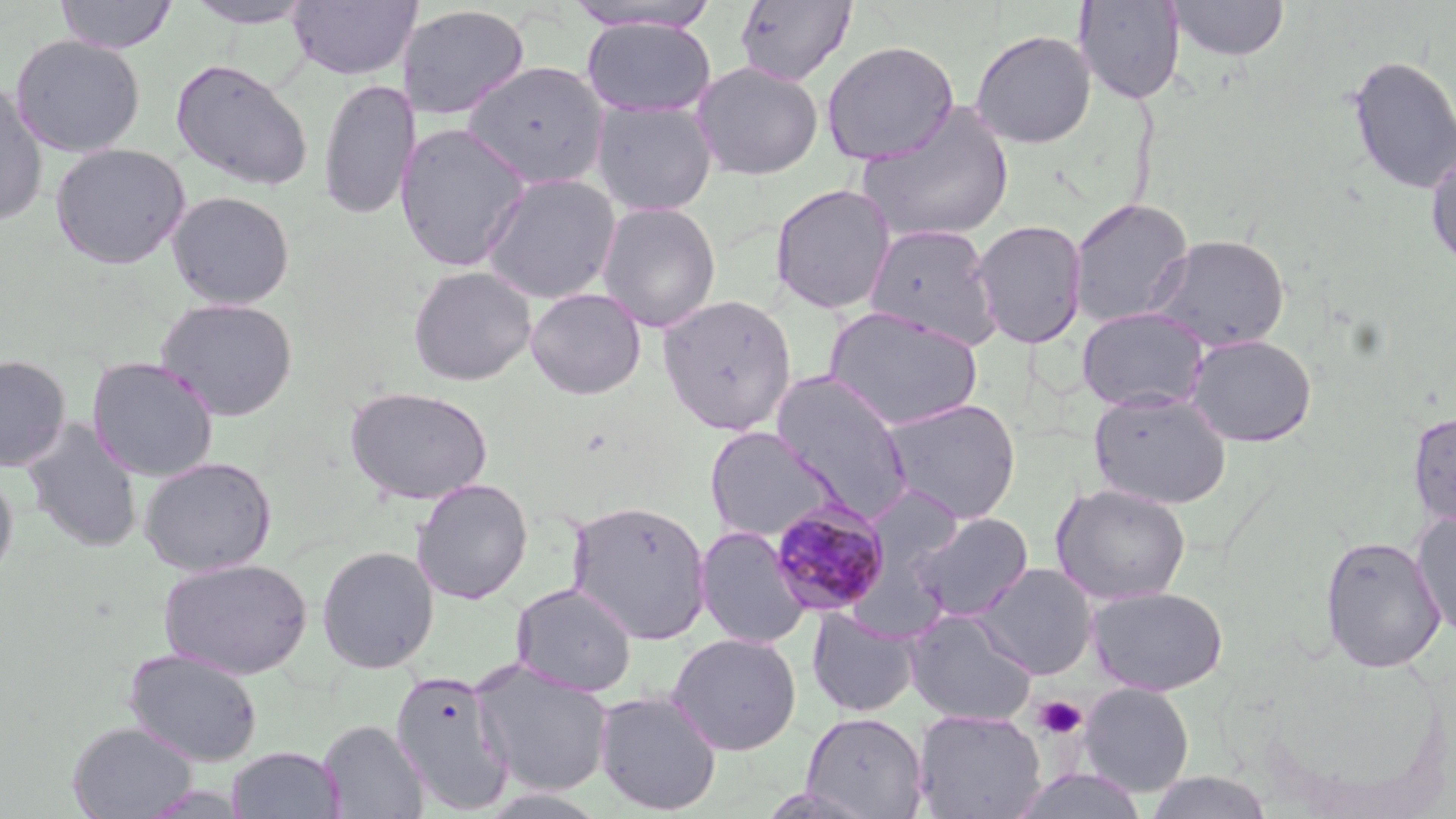 Approximate bounding boxes as named x1/y1/x2/y2 corners in pixels. Plasmodium malariae-infected red blood cell locations: (x1=769, y1=497, x2=892, y2=618). Uninfected red blood cell locations: (x1=55, y1=0, x2=178, y2=54), (x1=183, y1=0, x2=318, y2=28), (x1=287, y1=0, x2=421, y2=81), (x1=560, y1=1, x2=725, y2=34), (x1=734, y1=1, x2=856, y2=86), (x1=1074, y1=1, x2=1186, y2=104), (x1=1168, y1=1, x2=1289, y2=61), (x1=399, y1=4, x2=530, y2=120), (x1=581, y1=18, x2=716, y2=118), (x1=970, y1=28, x2=1096, y2=149), (x1=10, y1=34, x2=146, y2=157), (x1=821, y1=40, x2=959, y2=166), (x1=1346, y1=54, x2=1456, y2=196), (x1=170, y1=58, x2=313, y2=192), (x1=463, y1=60, x2=610, y2=190), (x1=691, y1=60, x2=824, y2=180), (x1=317, y1=77, x2=419, y2=222), (x1=0, y1=81, x2=48, y2=225), (x1=591, y1=99, x2=717, y2=216), (x1=857, y1=103, x2=1015, y2=245), (x1=395, y1=121, x2=532, y2=272), (x1=50, y1=142, x2=190, y2=269), (x1=1425, y1=147, x2=1456, y2=272), (x1=479, y1=172, x2=621, y2=305), (x1=769, y1=183, x2=896, y2=315), (x1=167, y1=190, x2=296, y2=310), (x1=1069, y1=198, x2=1194, y2=328), (x1=597, y1=202, x2=721, y2=332), (x1=971, y1=219, x2=1088, y2=349), (x1=864, y1=223, x2=1001, y2=349), (x1=1149, y1=234, x2=1290, y2=352), (x1=407, y1=265, x2=537, y2=386), (x1=525, y1=288, x2=647, y2=399), (x1=657, y1=294, x2=796, y2=436), (x1=156, y1=297, x2=298, y2=421), (x1=823, y1=305, x2=984, y2=431), (x1=1076, y1=306, x2=1210, y2=412), (x1=1186, y1=333, x2=1317, y2=447), (x1=0, y1=354, x2=71, y2=471), (x1=86, y1=356, x2=219, y2=482), (x1=771, y1=371, x2=916, y2=521), (x1=345, y1=385, x2=493, y2=505), (x1=1088, y1=390, x2=1232, y2=509), (x1=881, y1=398, x2=1022, y2=524), (x1=1408, y1=410, x2=1456, y2=530), (x1=22, y1=419, x2=144, y2=553), (x1=705, y1=426, x2=840, y2=543), (x1=138, y1=456, x2=277, y2=576), (x1=0, y1=469, x2=18, y2=585), (x1=411, y1=478, x2=533, y2=604), (x1=1050, y1=482, x2=1192, y2=605), (x1=858, y1=484, x2=967, y2=602), (x1=567, y1=499, x2=712, y2=644), (x1=1411, y1=511, x2=1456, y2=638), (x1=909, y1=512, x2=1033, y2=622), (x1=695, y1=525, x2=810, y2=649), (x1=1319, y1=535, x2=1447, y2=673), (x1=316, y1=545, x2=439, y2=674), (x1=158, y1=557, x2=313, y2=679), (x1=975, y1=562, x2=1097, y2=679), (x1=511, y1=582, x2=638, y2=697), (x1=1087, y1=586, x2=1228, y2=696), (x1=807, y1=608, x2=920, y2=718), (x1=906, y1=609, x2=1037, y2=726), (x1=667, y1=632, x2=802, y2=755), (x1=124, y1=648, x2=263, y2=766), (x1=470, y1=660, x2=615, y2=797), (x1=390, y1=669, x2=515, y2=814), (x1=1079, y1=682, x2=1194, y2=797), (x1=593, y1=689, x2=723, y2=815), (x1=913, y1=709, x2=1047, y2=819), (x1=800, y1=711, x2=928, y2=818), (x1=318, y1=718, x2=429, y2=819), (x1=68, y1=721, x2=197, y2=818), (x1=227, y1=746, x2=345, y2=819), (x1=1144, y1=771, x2=1273, y2=818). Platelet locations: (x1=1033, y1=695, x2=1087, y2=740). Slide-level diagnosis: Plasmodium malariae. May-Grünwald-Giemsa stain. One field of a larger specimen. Thin blood film. Light microscopy. 1000x magnification. Image is 1456×819 pixels.